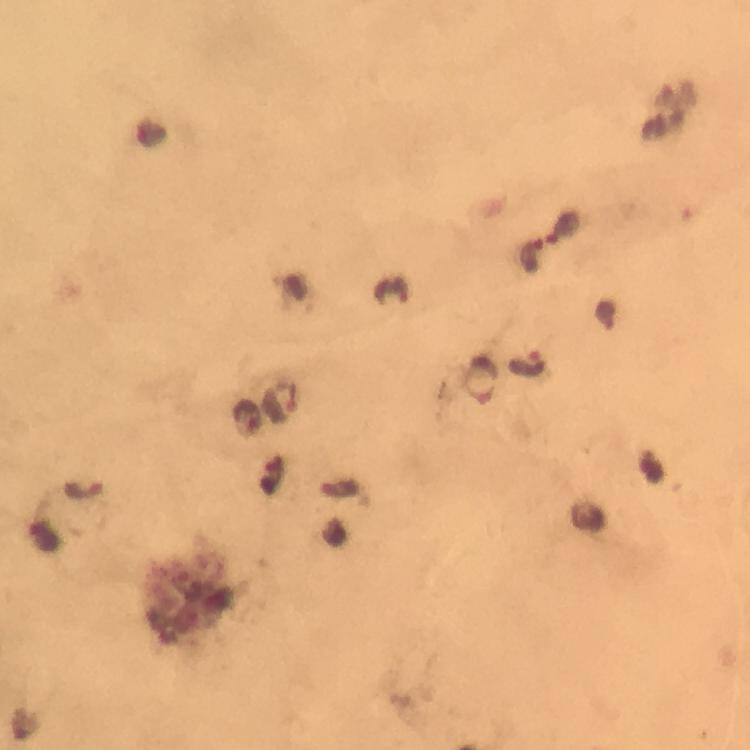

malaria parasite locations = approximate centers as (x, y) in pixels: (566, 224), (533, 254), (393, 293), (605, 313), (528, 363), (479, 380), (281, 402), (246, 418), (653, 468), (273, 474), (82, 489), (340, 490)
context = from a diagnostic examination for malaria
image size = 750×750 pixels
immersion oil = used
cropped from = one field of view
stain = Giemsa
magnification = 100x
capture = smartphone photograph through a microscope
preparation = thick smear